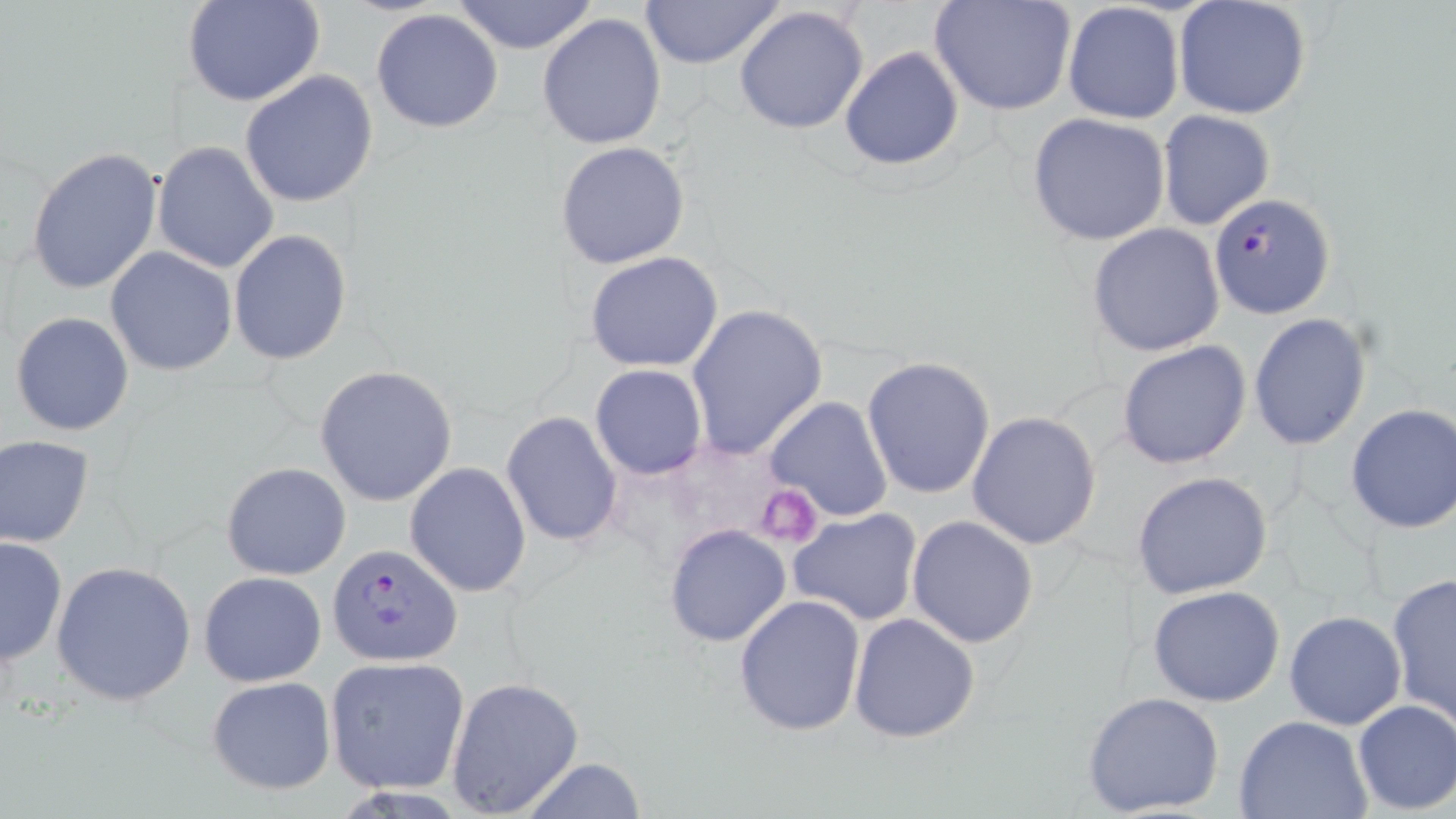

Approximate bounding boxes as (x1, y1, x2, y2) in pixels. Platelet locations: (756, 486, 824, 547). Uninfected red blood cell locations: (183, 0, 327, 108), (450, 0, 601, 55), (637, 0, 786, 71), (928, 0, 1079, 118), (1173, 0, 1313, 121), (1062, 2, 1185, 123), (734, 6, 871, 136), (371, 8, 505, 133), (537, 13, 666, 150), (838, 45, 966, 171), (239, 70, 379, 208), (1157, 110, 1276, 231), (1025, 112, 1172, 248), (554, 141, 690, 269), (152, 142, 279, 274), (25, 146, 164, 295), (1085, 222, 1227, 357), (228, 228, 352, 365), (105, 247, 237, 376), (585, 251, 726, 373), (685, 303, 828, 461), (11, 311, 135, 435), (1248, 312, 1371, 451), (1116, 339, 1253, 468), (861, 356, 996, 500), (314, 364, 459, 508), (591, 364, 707, 479), (765, 396, 894, 522), (1344, 404, 1456, 536), (966, 411, 1102, 550), (501, 412, 623, 547), (0, 434, 95, 547), (222, 462, 351, 581), (404, 462, 532, 597), (1132, 471, 1274, 599), (788, 508, 923, 626), (907, 516, 1040, 648), (663, 523, 792, 647), (0, 536, 67, 669), (50, 560, 196, 706), (198, 570, 326, 687), (1386, 573, 1456, 729), (1147, 584, 1286, 707), (733, 595, 866, 735), (1283, 610, 1408, 730), (849, 612, 980, 743), (324, 656, 471, 795), (206, 675, 337, 796), (444, 675, 585, 818), (1081, 690, 1225, 817), (1351, 699, 1456, 815), (1232, 715, 1373, 819), (517, 757, 649, 819). Plasmodium falciparum-infected red blood cell locations: (1208, 192, 1334, 321), (327, 543, 462, 669). Slide-level diagnosis: Plasmodium falciparum. Thin blood smear. May-Grünwald-Giemsa-stained preparation. Image is 1456×819 pixels. Optical microscopy. Captured at 1000x magnification. One field of a larger specimen.